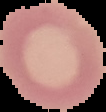

Image is 106×112 pixels. From a thin blood film. Segmented cell region on a black background. Malaria status: uninfected.